Assess this cell for malaria.
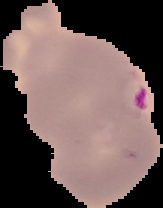

It is parasitized.

From a thin blood film. Segmented cell region on a black background. Image is 163×208 pixels.